Assess this cell for malaria.
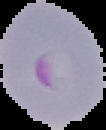

It is parasitized.

From a thin blood smear. Image is 106×130 pixels. Cell region segmented out of the field of view; the surrounding area is masked to black.